Outline platelets.
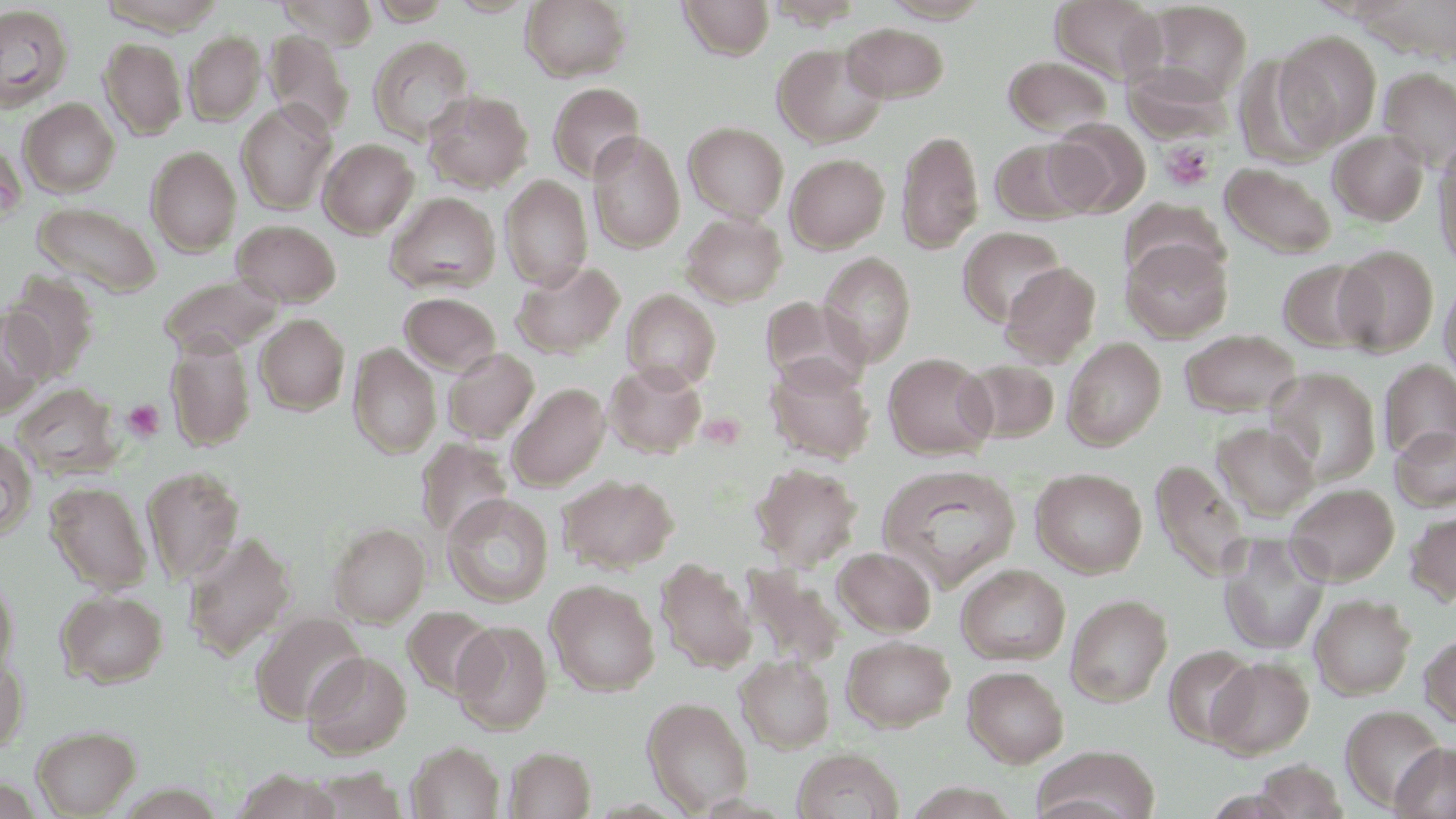

Approximate bounding boxes as (x1,y1)-(x2,y2) corner pairs in pixels.
Platelets: (1160,141)-(1216,191), (123,399)-(166,441).

slide-level diagnosis = negative for blood parasites
image size = 1456×819 pixels
uninfected red blood cell locations = approximate bounding boxes as (x1,y1)-(x2,y2) corner pairs in pixels: (99,0)-(226,34), (276,0)-(379,49), (369,0)-(455,25), (445,0)-(536,17), (521,0)-(632,82), (677,0)-(775,60), (880,0)-(992,22), (1051,0)-(1166,85), (1133,2)-(1253,106), (0,4)-(73,111), (841,22)-(949,103), (264,30)-(354,136), (1275,30)-(1382,147), (184,31)-(265,124), (368,35)-(476,144), (98,37)-(187,140), (772,43)-(888,147), (1003,56)-(1113,137), (1377,66)-(1456,170), (547,82)-(647,183), (423,90)-(533,193), (19,98)-(120,197), (236,101)-(337,215), (1046,119)-(1148,217), (683,122)-(790,222), (897,129)-(984,255), (1329,130)-(1429,225), (588,132)-(685,252), (319,139)-(419,238), (990,139)-(1090,224), (1433,141)-(1456,273), (146,146)-(241,256), (785,153)-(889,253), (1220,161)-(1338,259), (500,175)-(593,291), (385,192)-(501,295), (1121,199)-(1226,286), (33,201)-(161,297), (682,211)-(786,307), (231,219)-(341,306), (957,226)-(1067,327), (1121,237)-(1232,342), (1334,245)-(1439,356), (818,252)-(915,367), (1278,259)-(1381,352), (511,261)-(624,358), (999,262)-(1101,366), (3,271)-(100,381), (1439,273)-(1456,389), (159,274)-(285,357), (621,289)-(721,391), (399,292)-(502,375), (760,296)-(869,393), (0,306)-(51,419), (255,314)-(349,415), (1180,329)-(1303,418), (165,333)-(256,452), (1062,337)-(1166,450), (347,343)-(441,459), (442,348)-(539,443), (884,353)-(995,459), (765,354)-(875,464), (958,359)-(1059,443), (1378,359)-(1456,463), (604,362)-(706,458), (1266,368)-(1381,485), (507,383)-(610,490), (11,384)-(122,478), (1211,421)-(1319,522), (1390,425)-(1456,511), (0,436)-(37,540), (415,438)-(513,542), (1151,458)-(1250,582), (751,463)-(862,570), (877,464)-(1022,589), (141,466)-(245,585), (1030,467)-(1147,577), (557,474)-(678,573), (45,481)-(152,593), (1284,482)-(1400,585), (442,493)-(553,607), (1405,507)-(1456,606), (329,523)-(430,626), (182,531)-(296,660), (1219,532)-(1330,656), (833,547)-(936,636), (655,557)-(756,673), (957,564)-(1071,664), (741,566)-(844,671), (0,572)-(18,681), (546,579)-(659,696), (56,589)-(168,687), (1065,593)-(1173,707), (1310,594)-(1415,700), (403,606)-(497,699), (250,612)-(367,724), (451,621)-(552,734), (1419,633)-(1456,729), (841,636)-(955,731), (1164,645)-(1259,747), (302,651)-(412,759), (735,654)-(835,753), (0,655)-(27,753), (1207,656)-(1314,759), (962,666)-(1069,767), (642,696)-(754,815), (1340,705)-(1446,810), (32,725)-(141,817), (406,741)-(505,819), (1390,742)-(1456,819), (505,746)-(596,819), (792,747)-(903,819), (1033,747)-(1161,819), (1253,760)-(1348,817), (306,767)-(408,819), (233,770)-(341,819)
magnification = 1000x
stain = May-Grünwald-Giemsa
field of view = single
modality = optical microscopy
preparation = thin blood smear